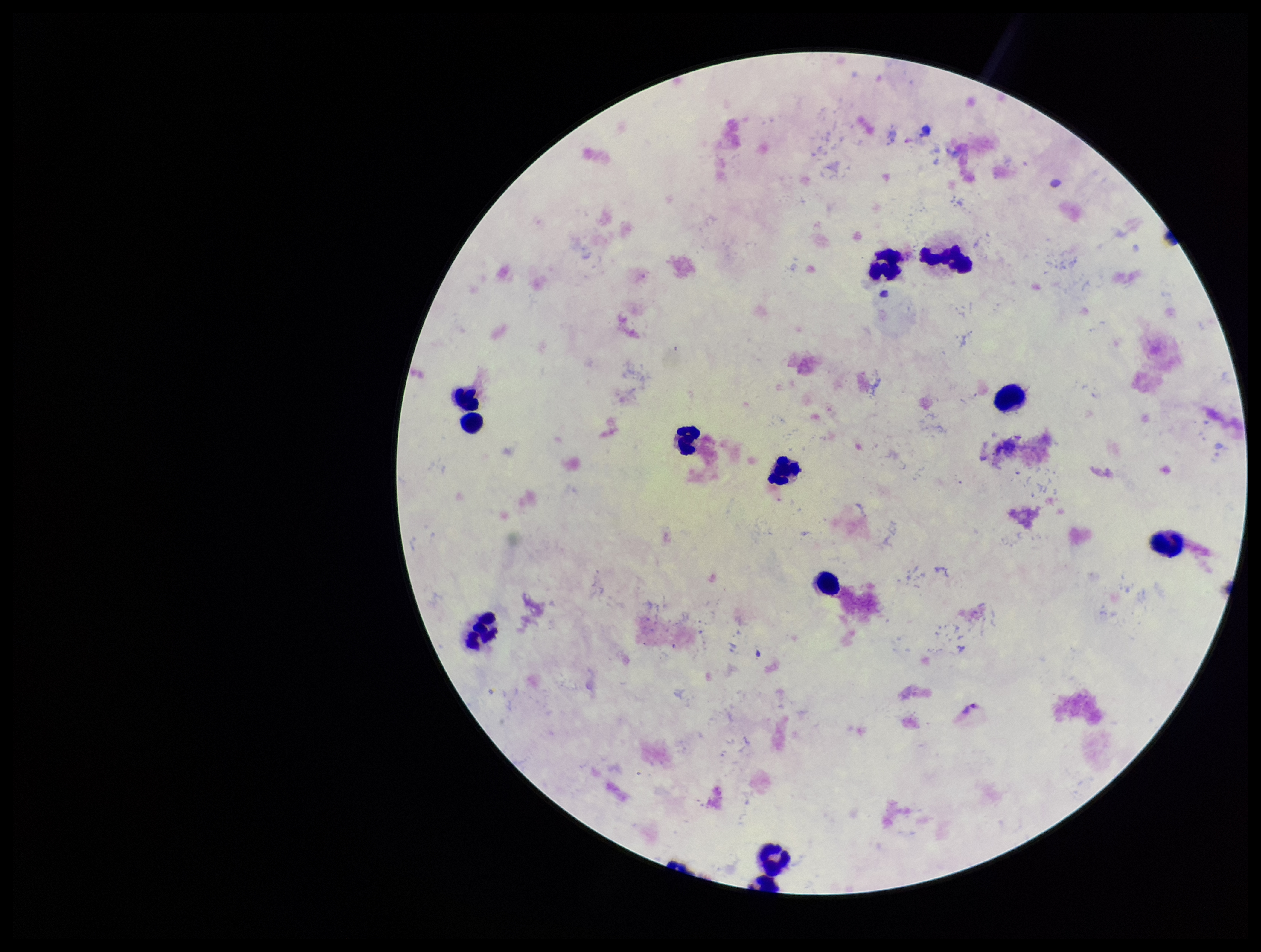

{
  "species_reported_for_this_patient": "Plasmodium vivax",
  "image_size": "1261×952 pixels",
  "leukocyte_count": 12,
  "stain": "Giemsa",
  "preparation": "thick",
  "capture": "smartphone photograph through the microscope eyepiece",
  "plasmodium_parasites": "none identified",
  "field_of_view": "one from this slide",
  "patient_malaria_status": "positive",
  "parasite_count": 0
}